Comment on the morphology of the red blood cells.
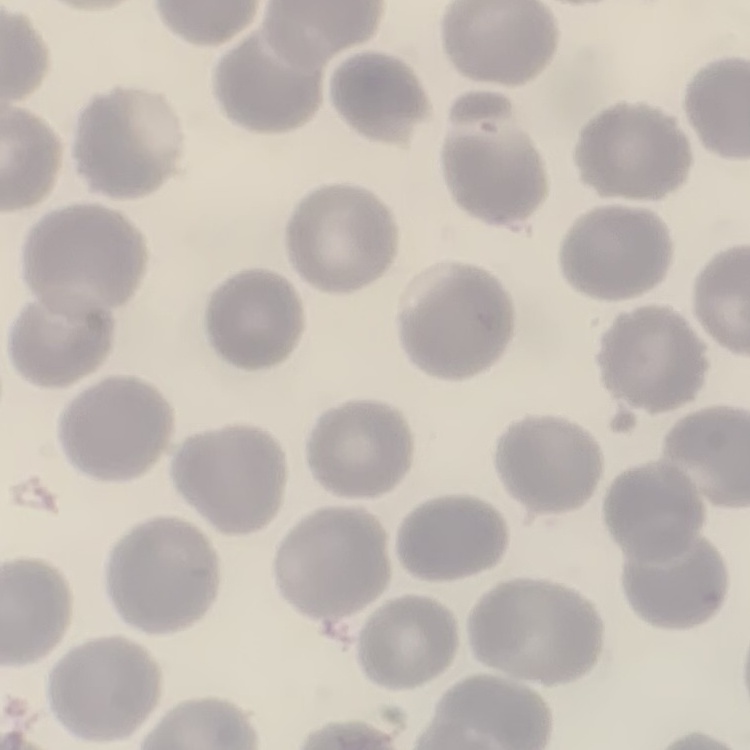
They show no rouleaux formation.

Thin blood film. Stained with either Field's or Giemsa. Square crop of a larger photomicrograph.